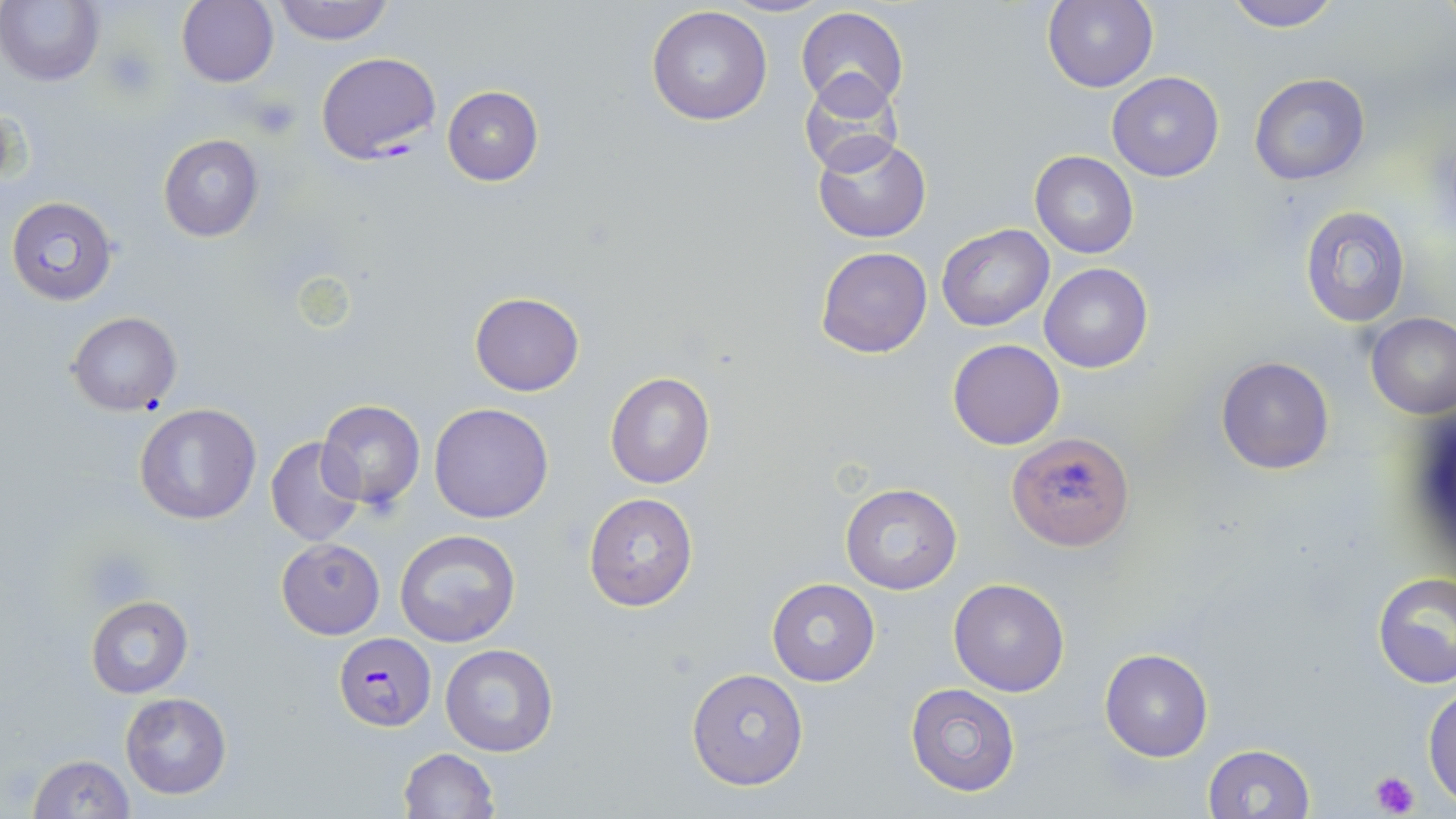

Summary:
  - Coordinate format: approximate bounding boxes as [x1, y1, x2, y2] in pixels
  - Platelet locations: [103, 46, 160, 101], [247, 92, 301, 141], [85, 551, 148, 603], [1371, 771, 1420, 816]
  - Plasmodium falciparum-infected red blood cell locations: [315, 52, 439, 164], [333, 633, 434, 732]
  - Uninfected red blood cell locations: [177, 0, 278, 87], [272, 0, 395, 45], [720, 0, 831, 18], [1043, 0, 1159, 93], [1222, 0, 1343, 33], [0, 1, 104, 86], [646, 5, 773, 126], [795, 7, 909, 113], [799, 69, 908, 177], [1106, 72, 1224, 182], [1249, 73, 1370, 187], [442, 86, 544, 185], [158, 134, 264, 242], [811, 134, 931, 243], [1030, 150, 1139, 258], [7, 197, 119, 305], [1299, 205, 1412, 328], [936, 223, 1054, 331], [815, 246, 932, 357], [1040, 261, 1152, 373], [469, 291, 585, 396], [66, 312, 181, 416], [1365, 312, 1456, 419], [947, 338, 1064, 450], [1215, 355, 1335, 475], [604, 372, 715, 489], [316, 396, 426, 515], [430, 402, 554, 524], [135, 403, 261, 524], [1008, 432, 1135, 551], [264, 435, 366, 547], [840, 484, 963, 595], [583, 493, 699, 610], [394, 528, 521, 648], [276, 537, 384, 639], [1373, 573, 1456, 692], [948, 577, 1071, 697], [766, 578, 879, 687], [86, 595, 194, 698], [440, 643, 560, 757], [1100, 649, 1214, 762], [686, 667, 809, 790], [1423, 682, 1456, 804], [905, 683, 1020, 796], [119, 690, 233, 800], [1202, 744, 1315, 819], [395, 748, 500, 819], [25, 754, 136, 818]
  - Slide-level diagnosis: Plasmodium falciparum
  - Field of view: one of a larger specimen
  - Preparation: thin blood film
  - Stain: May-Grünwald-Giemsa
  - Modality: optical microscopy
  - Image size: 1456×819 pixels
  - Magnification: 1000x